Name the parasite shown.
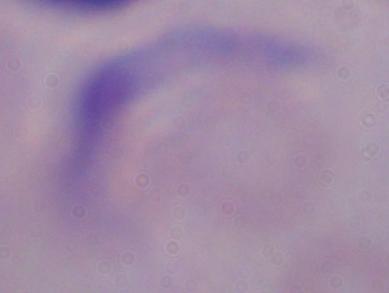

This is a trypanosome.

magnification = 1000x
modality = photomicrograph